Identify the blood parasite species.
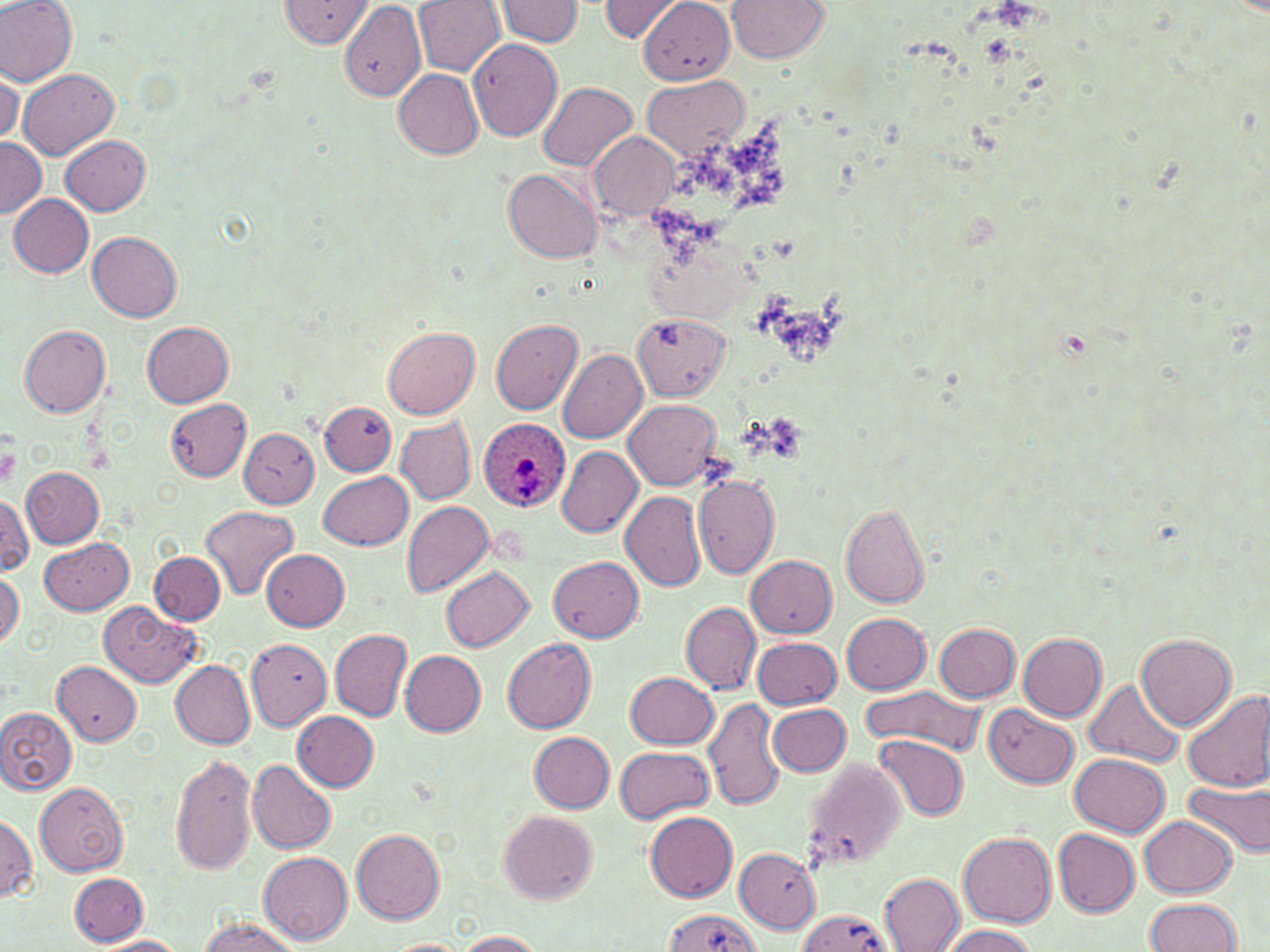
Plasmodium ovale.

image size = 1270×952 pixels
field of view = one of a larger specimen
Plasmodium ovale-infected red blood cell locations = approximate bounding boxes as named x1/y1/x2/y2 corners in pixels: (x1=478, y1=417, x2=570, y2=513)
magnification = 1000x
modality = light microscopy
platelet locations = approximate bounding boxes as named x1/y1/x2/y2 corners in pixels: (x1=0, y1=443, x2=21, y2=489)
stain = May-Grünwald-Giemsa
uninfected red blood cell locations = approximate bounding boxes as named x1/y1/x2/y2 corners in pixels: (x1=0, y1=0, x2=77, y2=86), (x1=280, y1=0, x2=373, y2=49), (x1=413, y1=0, x2=504, y2=76), (x1=496, y1=0, x2=584, y2=46), (x1=598, y1=0, x2=685, y2=43), (x1=728, y1=0, x2=829, y2=63), (x1=339, y1=1, x2=426, y2=102), (x1=636, y1=1, x2=738, y2=84), (x1=468, y1=37, x2=563, y2=141), (x1=19, y1=68, x2=119, y2=161), (x1=1, y1=69, x2=22, y2=146), (x1=395, y1=70, x2=483, y2=159), (x1=642, y1=75, x2=744, y2=162), (x1=538, y1=83, x2=638, y2=171), (x1=590, y1=133, x2=678, y2=218), (x1=60, y1=134, x2=151, y2=214), (x1=0, y1=137, x2=45, y2=221), (x1=504, y1=168, x2=603, y2=263), (x1=8, y1=193, x2=94, y2=277), (x1=88, y1=232, x2=182, y2=321), (x1=634, y1=313, x2=731, y2=401), (x1=492, y1=319, x2=582, y2=414), (x1=142, y1=321, x2=233, y2=405), (x1=19, y1=325, x2=110, y2=417), (x1=382, y1=326, x2=480, y2=418), (x1=558, y1=348, x2=647, y2=442), (x1=167, y1=398, x2=251, y2=481), (x1=624, y1=399, x2=722, y2=488), (x1=320, y1=403, x2=396, y2=475), (x1=394, y1=415, x2=475, y2=505), (x1=240, y1=427, x2=320, y2=509), (x1=556, y1=446, x2=642, y2=538), (x1=21, y1=466, x2=105, y2=546), (x1=320, y1=471, x2=413, y2=550), (x1=692, y1=474, x2=780, y2=579), (x1=620, y1=490, x2=706, y2=592), (x1=1, y1=493, x2=33, y2=575), (x1=401, y1=501, x2=496, y2=598), (x1=840, y1=503, x2=931, y2=609), (x1=201, y1=505, x2=299, y2=599), (x1=40, y1=538, x2=133, y2=616), (x1=262, y1=550, x2=349, y2=630), (x1=151, y1=553, x2=225, y2=625), (x1=745, y1=555, x2=837, y2=637), (x1=548, y1=556, x2=643, y2=642), (x1=441, y1=565, x2=533, y2=651), (x1=0, y1=573, x2=24, y2=648), (x1=680, y1=600, x2=760, y2=694), (x1=100, y1=601, x2=201, y2=688), (x1=842, y1=613, x2=931, y2=694), (x1=933, y1=623, x2=1021, y2=702), (x1=330, y1=629, x2=412, y2=721), (x1=1017, y1=632, x2=1107, y2=721), (x1=1136, y1=632, x2=1235, y2=729), (x1=752, y1=636, x2=841, y2=709), (x1=502, y1=638, x2=597, y2=734), (x1=245, y1=640, x2=332, y2=733), (x1=400, y1=651, x2=485, y2=736), (x1=171, y1=659, x2=255, y2=749), (x1=53, y1=660, x2=142, y2=746), (x1=626, y1=671, x2=719, y2=749), (x1=1085, y1=680, x2=1183, y2=765), (x1=862, y1=684, x2=987, y2=756), (x1=1182, y1=688, x2=1270, y2=794), (x1=703, y1=696, x2=783, y2=812), (x1=768, y1=703, x2=850, y2=776), (x1=985, y1=706, x2=1079, y2=787), (x1=0, y1=707, x2=77, y2=796), (x1=294, y1=711, x2=379, y2=791), (x1=529, y1=732, x2=614, y2=812), (x1=875, y1=735, x2=969, y2=821), (x1=615, y1=747, x2=714, y2=823), (x1=172, y1=754, x2=257, y2=877), (x1=1071, y1=754, x2=1170, y2=837), (x1=247, y1=759, x2=335, y2=854), (x1=798, y1=759, x2=905, y2=874), (x1=1184, y1=779, x2=1270, y2=860), (x1=34, y1=782, x2=130, y2=876), (x1=498, y1=810, x2=598, y2=904), (x1=645, y1=811, x2=737, y2=902), (x1=1139, y1=816, x2=1236, y2=897), (x1=0, y1=817, x2=36, y2=901), (x1=352, y1=828, x2=445, y2=925), (x1=1053, y1=829, x2=1140, y2=916), (x1=958, y1=831, x2=1056, y2=927), (x1=734, y1=848, x2=821, y2=932), (x1=258, y1=851, x2=353, y2=945), (x1=70, y1=873, x2=147, y2=945), (x1=880, y1=874, x2=965, y2=951), (x1=1145, y1=898, x2=1243, y2=952), (x1=661, y1=910, x2=759, y2=952), (x1=797, y1=910, x2=895, y2=952), (x1=198, y1=919, x2=301, y2=952), (x1=939, y1=924, x2=1040, y2=952), (x1=450, y1=931, x2=550, y2=951), (x1=94, y1=936, x2=186, y2=952), (x1=380, y1=939, x2=475, y2=952)
preparation = thin blood film